Locate every Plasmodium parasite.
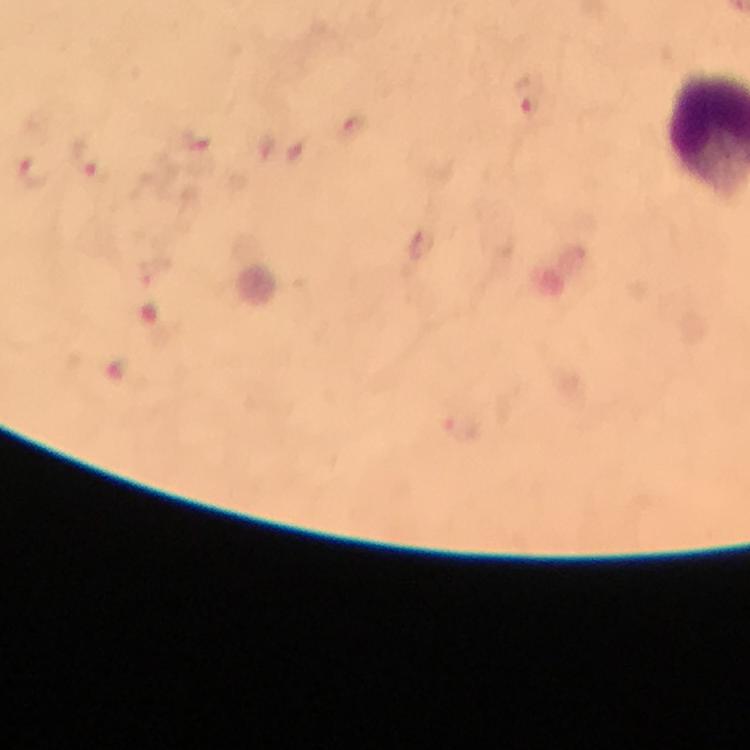

Approximate centers as (x, y) in pixels.
Plasmodium parasites: (529, 96), (350, 128), (89, 162), (35, 171), (421, 244).

immersion oil = used
cropped from = a single field of view
stain = Giemsa
preparation = thick blood smear
capture = smartphone mounted on the microscope
context = from a diagnostic examination for malaria
image size = 750×750 pixels
magnification = 100x